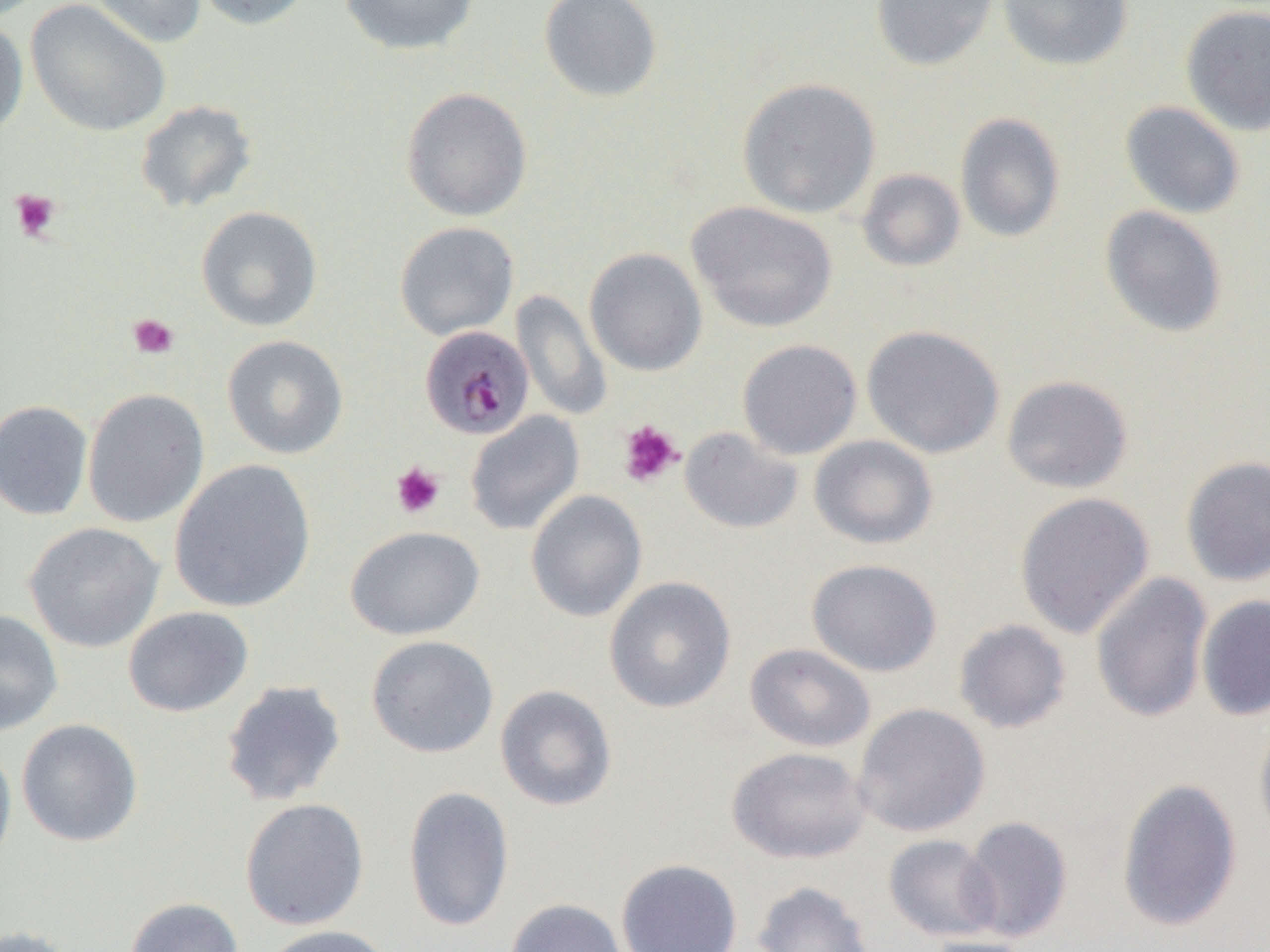
Approximate bounding boxes as (x1,y1)-(x2,y2) corner pairs in pixels. Uninfected red blood cell locations: (89,0)-(207,49), (191,0)-(315,31), (339,0)-(480,55), (539,0)-(663,103), (870,0)-(1000,72), (997,0)-(1134,71), (26,1)-(171,137), (1180,3)-(1270,136), (0,16)-(29,139), (737,78)-(881,219), (400,87)-(533,221), (134,99)-(258,213), (1120,101)-(1246,219), (955,112)-(1066,242), (856,168)-(966,272), (687,201)-(838,333), (196,206)-(323,332), (1099,206)-(1228,338), (394,221)-(519,340), (584,247)-(708,377), (511,290)-(612,421), (861,324)-(1005,459), (222,335)-(349,459), (737,338)-(862,460), (1001,375)-(1134,494), (82,388)-(210,527), (0,400)-(93,521), (465,411)-(585,536), (679,426)-(803,534), (808,434)-(938,550), (1180,455)-(1270,587), (169,459)-(316,613), (526,490)-(647,622), (1014,492)-(1155,639), (24,522)-(164,653), (345,525)-(486,641), (806,558)-(943,676), (1090,572)-(1213,724), (604,577)-(737,713), (1196,594)-(1270,721), (123,606)-(254,717), (0,608)-(63,736), (953,619)-(1072,734), (366,635)-(499,759), (745,642)-(876,753), (220,679)-(347,807), (494,684)-(618,811), (852,702)-(991,837), (1254,714)-(1270,846), (16,718)-(143,847), (0,737)-(17,874), (727,746)-(871,864), (1116,777)-(1243,932), (403,785)-(514,933), (239,797)-(370,931), (960,815)-(1073,942), (884,834)-(1002,942), (615,858)-(742,952), (752,881)-(875,952), (125,897)-(244,952), (505,898)-(627,952), (0,924)-(81,952), (260,924)-(394,952), (922,936)-(1039,952). Plasmodium malariae-infected red blood cell locations: (420,325)-(535,440). Platelet locations: (10,189)-(61,242), (127,314)-(179,360), (617,420)-(684,488), (391,461)-(446,520). Slide-level diagnosis: Plasmodium malariae. 1000x magnification. Single field of view. Thin blood smear. Optical microscopy. Image is 1270×952 pixels.